Give the position of every Plasmodium parasite and every leukocyte.
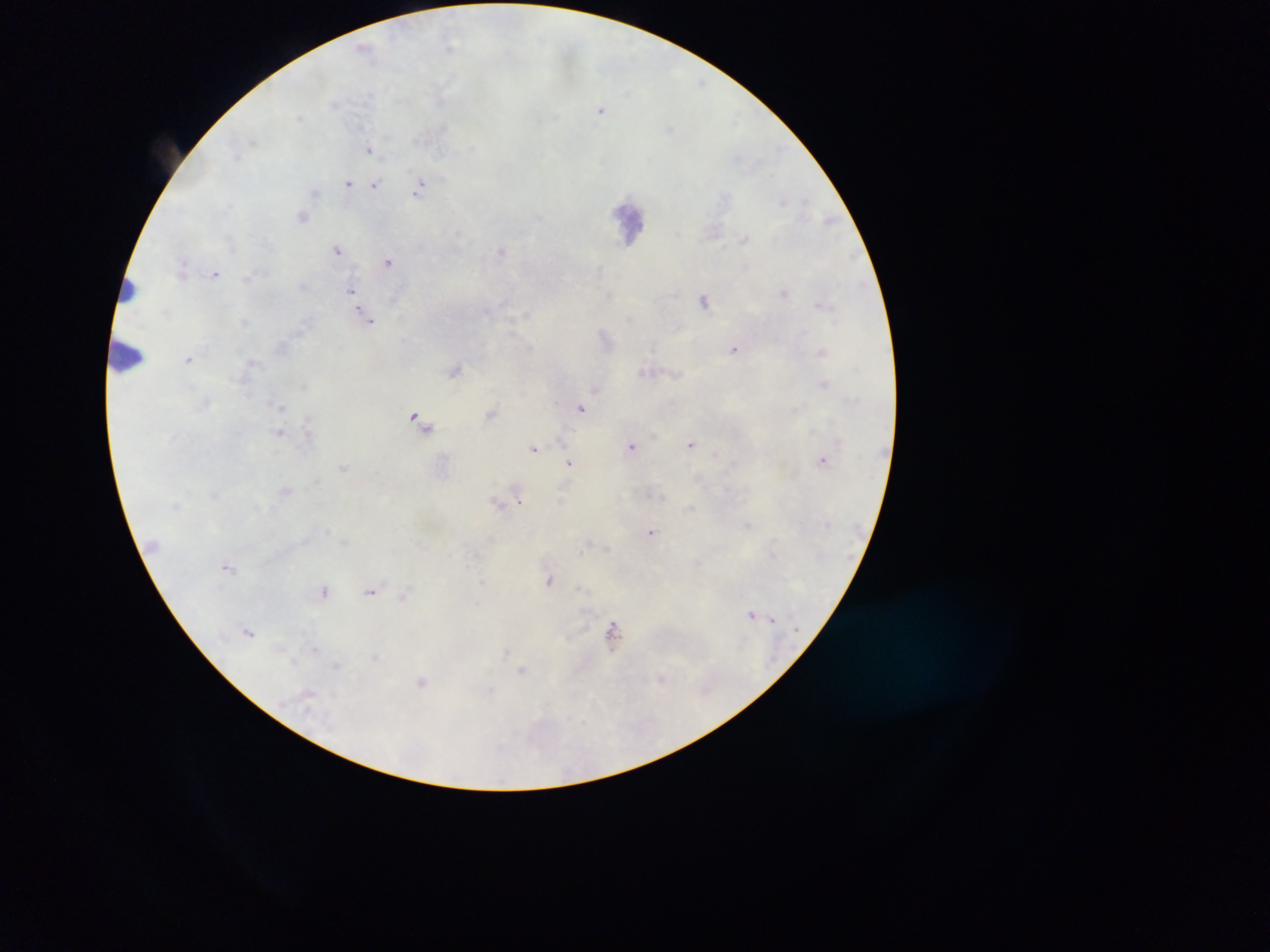

Approximate centers as [x, y] in pixels.
Plasmodium parasites: [451, 47], [364, 48], [601, 109], [369, 148], [349, 183], [374, 185], [420, 187], [315, 193], [302, 216], [338, 249], [501, 250], [388, 261], [216, 273], [352, 290], [785, 292], [705, 299], [366, 315], [245, 321], [606, 337], [735, 347], [821, 351], [188, 359], [455, 368], [647, 372], [824, 384], [596, 390], [281, 406], [582, 408], [490, 413], [420, 419], [280, 432], [559, 438], [692, 443], [632, 447], [535, 448], [823, 459], [569, 462], [345, 467], [287, 489], [519, 501], [498, 503], [749, 525], [652, 532], [589, 543], [607, 549], [228, 566], [550, 580], [482, 582], [324, 590], [370, 590], [402, 597], [752, 615], [773, 619], [612, 630], [250, 631], [521, 670], [662, 678], [422, 681].
Leukocytes: [629, 220], [128, 290], [126, 355].

capture = mobile-phone photograph through a microscope
preparation = thick blood smear
field of view = single
country = Ghana
image size = 1270×952 pixels